State which parasite is depicted.
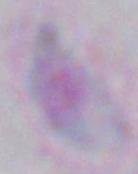

Toxoplasma gondii.

Micrograph. 1000x magnification.